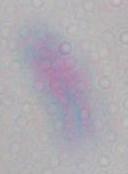 Captured at 1000x magnification. Micrograph. Toxoplasma gondii is seen.